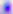

modality = photomicrograph
identification = Toxoplasma gondii
magnification = 400x